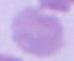 Captured at 1000x magnification. An erythrocyte is shown. Micrograph.